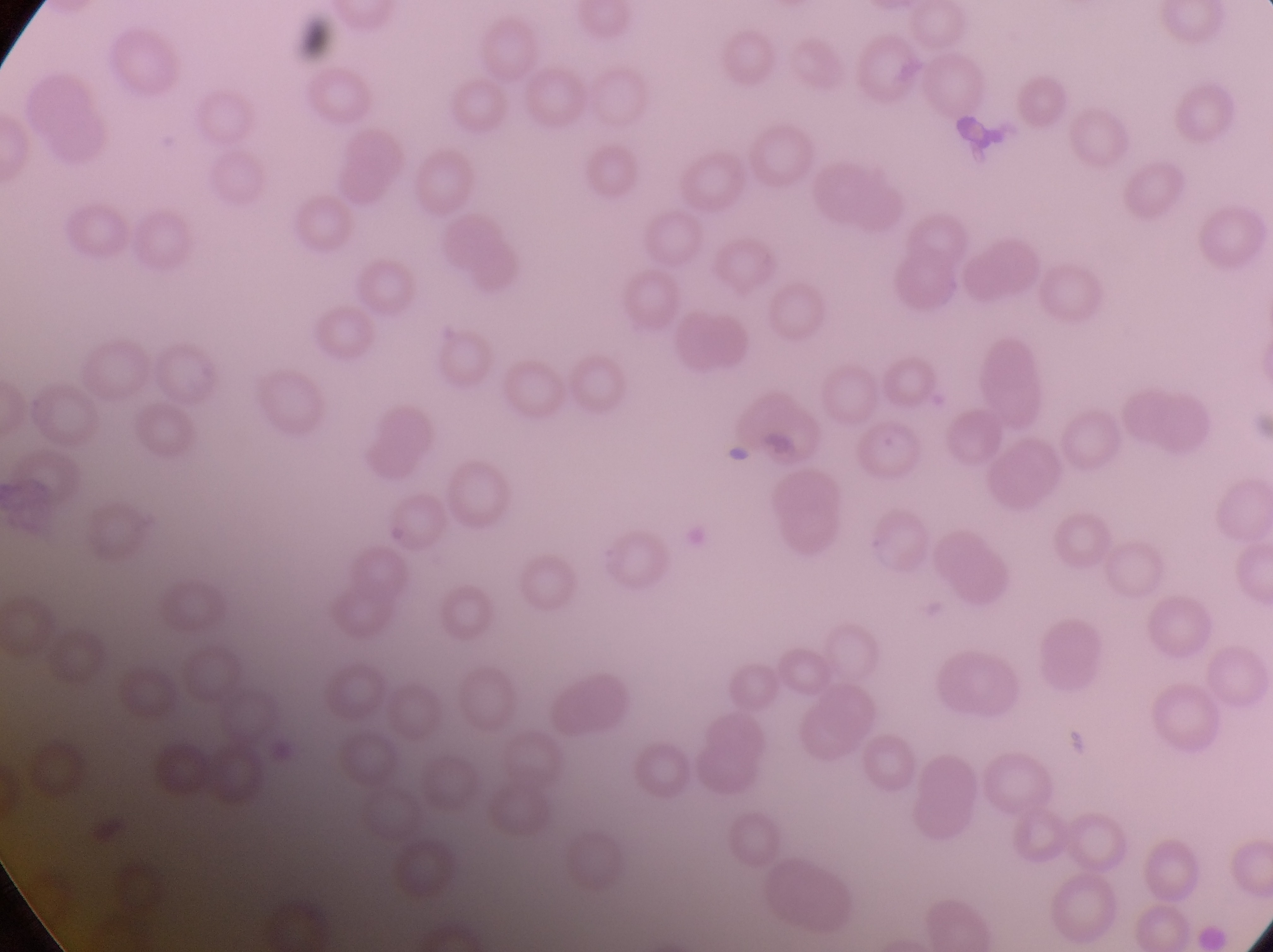
Approximate bounding boxes as left top right bottom in pixels. Parasitised red blood cell locations: 859 417 929 485. Artifact (platelet-like body, stain precipitate, or debris) locations: 759 422 801 470; 1066 725 1092 758. Image is 1273×952 pixels. Single field of view. Magnification of 1000x. Collected in Uganda. Thin blood film. Captured by a smartphone held over the eyepiece of an Olympus CX-23 microscope.